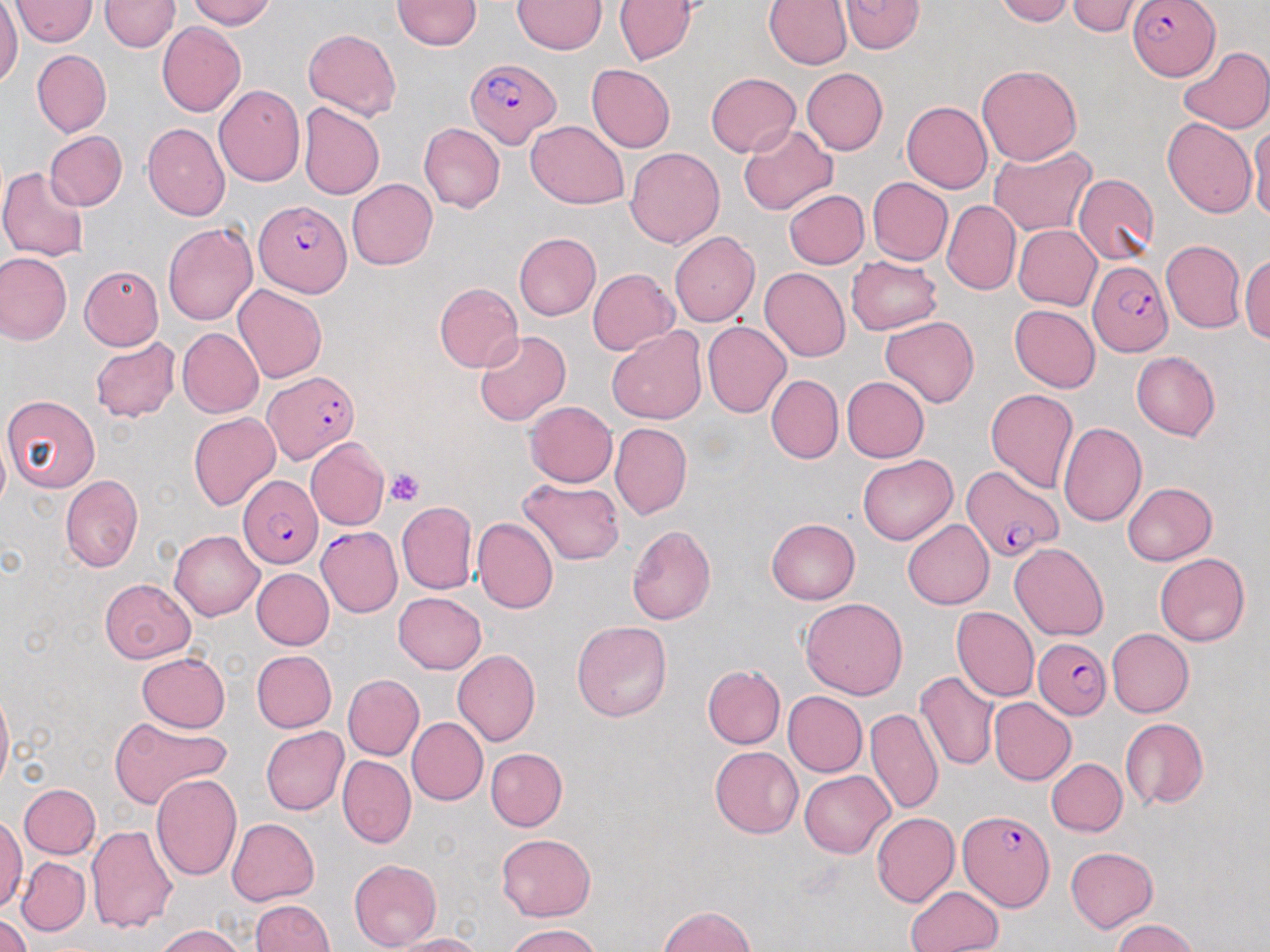

slide-level diagnosis = Plasmodium falciparum
magnification = 1000x
modality = light microscopy
image size = 1270×952 pixels
platelet locations = approximate bounding boxes as named x1/y1/x2/y2 corners in pixels: (x1=385, y1=468, x2=425, y2=505)
field of view = one of a larger specimen
preparation = thin blood film
stain = May-Grünwald-Giemsa
Plasmodium falciparum-infected red blood cell locations = approximate bounding boxes as named x1/y1/x2/y2 corners in pixels: (x1=1127, y1=0, x2=1219, y2=80), (x1=466, y1=58, x2=561, y2=149), (x1=253, y1=199, x2=351, y2=297), (x1=1087, y1=259, x2=1174, y2=355), (x1=264, y1=372, x2=360, y2=463), (x1=962, y1=466, x2=1061, y2=564), (x1=238, y1=475, x2=323, y2=568), (x1=315, y1=526, x2=402, y2=617), (x1=1033, y1=637, x2=1110, y2=719), (x1=958, y1=810, x2=1053, y2=909)
uninfected red blood cell locations = approximate bounding boxes as named x1/y1/x2/y2 corners in pixels: (x1=9, y1=0, x2=98, y2=45), (x1=101, y1=0, x2=178, y2=52), (x1=186, y1=0, x2=275, y2=29), (x1=392, y1=0, x2=481, y2=50), (x1=993, y1=0, x2=1075, y2=26), (x1=512, y1=1, x2=606, y2=54), (x1=613, y1=1, x2=696, y2=64), (x1=762, y1=1, x2=852, y2=69), (x1=839, y1=1, x2=924, y2=54), (x1=0, y1=2, x2=22, y2=89), (x1=1064, y1=2, x2=1147, y2=37), (x1=157, y1=22, x2=246, y2=116), (x1=303, y1=28, x2=402, y2=121), (x1=1179, y1=46, x2=1270, y2=134), (x1=32, y1=50, x2=112, y2=137), (x1=587, y1=64, x2=675, y2=152), (x1=977, y1=64, x2=1082, y2=166), (x1=801, y1=66, x2=888, y2=155), (x1=706, y1=72, x2=800, y2=156), (x1=213, y1=84, x2=305, y2=186), (x1=901, y1=101, x2=993, y2=193), (x1=298, y1=103, x2=385, y2=200), (x1=1163, y1=117, x2=1257, y2=217), (x1=526, y1=120, x2=630, y2=209), (x1=1248, y1=122, x2=1270, y2=219), (x1=144, y1=123, x2=231, y2=221), (x1=419, y1=123, x2=505, y2=213), (x1=739, y1=124, x2=837, y2=215), (x1=44, y1=131, x2=127, y2=210), (x1=625, y1=146, x2=725, y2=249), (x1=988, y1=146, x2=1096, y2=235), (x1=0, y1=167, x2=91, y2=261), (x1=1073, y1=174, x2=1160, y2=264), (x1=867, y1=177, x2=952, y2=264), (x1=346, y1=179, x2=437, y2=270), (x1=784, y1=190, x2=870, y2=269), (x1=941, y1=200, x2=1020, y2=295), (x1=163, y1=223, x2=258, y2=325), (x1=1013, y1=224, x2=1101, y2=310), (x1=670, y1=232, x2=761, y2=327), (x1=513, y1=233, x2=601, y2=321), (x1=1161, y1=240, x2=1245, y2=333), (x1=0, y1=251, x2=72, y2=345), (x1=1240, y1=253, x2=1269, y2=343), (x1=846, y1=255, x2=941, y2=336), (x1=79, y1=265, x2=163, y2=350), (x1=588, y1=268, x2=678, y2=356), (x1=759, y1=268, x2=850, y2=361), (x1=435, y1=283, x2=523, y2=373), (x1=232, y1=284, x2=327, y2=384), (x1=1009, y1=305, x2=1100, y2=393), (x1=879, y1=316, x2=980, y2=407), (x1=702, y1=320, x2=791, y2=417), (x1=177, y1=328, x2=263, y2=417), (x1=608, y1=328, x2=707, y2=424), (x1=474, y1=331, x2=571, y2=426), (x1=89, y1=337, x2=181, y2=423), (x1=1132, y1=351, x2=1220, y2=440), (x1=766, y1=373, x2=843, y2=464), (x1=842, y1=376, x2=930, y2=462), (x1=985, y1=388, x2=1078, y2=493), (x1=2, y1=394, x2=101, y2=492), (x1=523, y1=400, x2=617, y2=486), (x1=189, y1=413, x2=280, y2=511), (x1=610, y1=422, x2=692, y2=520), (x1=1058, y1=422, x2=1146, y2=526), (x1=0, y1=432, x2=10, y2=515), (x1=305, y1=437, x2=389, y2=530), (x1=858, y1=455, x2=958, y2=545), (x1=61, y1=475, x2=142, y2=572), (x1=518, y1=477, x2=625, y2=565), (x1=1122, y1=482, x2=1218, y2=566), (x1=396, y1=500, x2=476, y2=594), (x1=472, y1=517, x2=558, y2=614), (x1=766, y1=518, x2=860, y2=604), (x1=902, y1=519, x2=994, y2=609), (x1=627, y1=524, x2=716, y2=624), (x1=170, y1=530, x2=264, y2=620), (x1=1010, y1=543, x2=1108, y2=640), (x1=1154, y1=553, x2=1250, y2=646), (x1=250, y1=568, x2=334, y2=650), (x1=100, y1=578, x2=195, y2=663), (x1=393, y1=591, x2=487, y2=673), (x1=799, y1=597, x2=908, y2=700), (x1=951, y1=607, x2=1040, y2=702), (x1=572, y1=620, x2=672, y2=722), (x1=1107, y1=628, x2=1194, y2=717), (x1=452, y1=649, x2=540, y2=747), (x1=251, y1=650, x2=337, y2=732), (x1=137, y1=652, x2=231, y2=732), (x1=701, y1=666, x2=785, y2=749), (x1=915, y1=671, x2=1000, y2=771), (x1=343, y1=675, x2=424, y2=760), (x1=0, y1=686, x2=12, y2=797), (x1=782, y1=690, x2=868, y2=777), (x1=988, y1=697, x2=1077, y2=786), (x1=865, y1=707, x2=943, y2=814), (x1=108, y1=715, x2=230, y2=810), (x1=407, y1=717, x2=488, y2=805), (x1=1120, y1=718, x2=1208, y2=810), (x1=261, y1=726, x2=350, y2=815), (x1=710, y1=746, x2=804, y2=838), (x1=487, y1=748, x2=568, y2=831), (x1=337, y1=754, x2=416, y2=849), (x1=1046, y1=758, x2=1127, y2=837), (x1=799, y1=770, x2=893, y2=857), (x1=150, y1=774, x2=243, y2=881), (x1=19, y1=784, x2=100, y2=858), (x1=871, y1=813, x2=959, y2=908), (x1=227, y1=818, x2=319, y2=905), (x1=0, y1=819, x2=26, y2=911), (x1=85, y1=825, x2=178, y2=933), (x1=496, y1=834, x2=596, y2=921), (x1=1065, y1=847, x2=1155, y2=931), (x1=16, y1=857, x2=90, y2=936), (x1=349, y1=859, x2=442, y2=950), (x1=906, y1=885, x2=1005, y2=951), (x1=249, y1=900, x2=334, y2=952), (x1=658, y1=905, x2=754, y2=952), (x1=0, y1=913, x2=33, y2=952), (x1=1110, y1=919, x2=1198, y2=952), (x1=154, y1=924, x2=245, y2=952), (x1=504, y1=924, x2=598, y2=952), (x1=390, y1=932, x2=484, y2=952)